Give the extent of all Plasmodium falciparum-infected red blood cells.
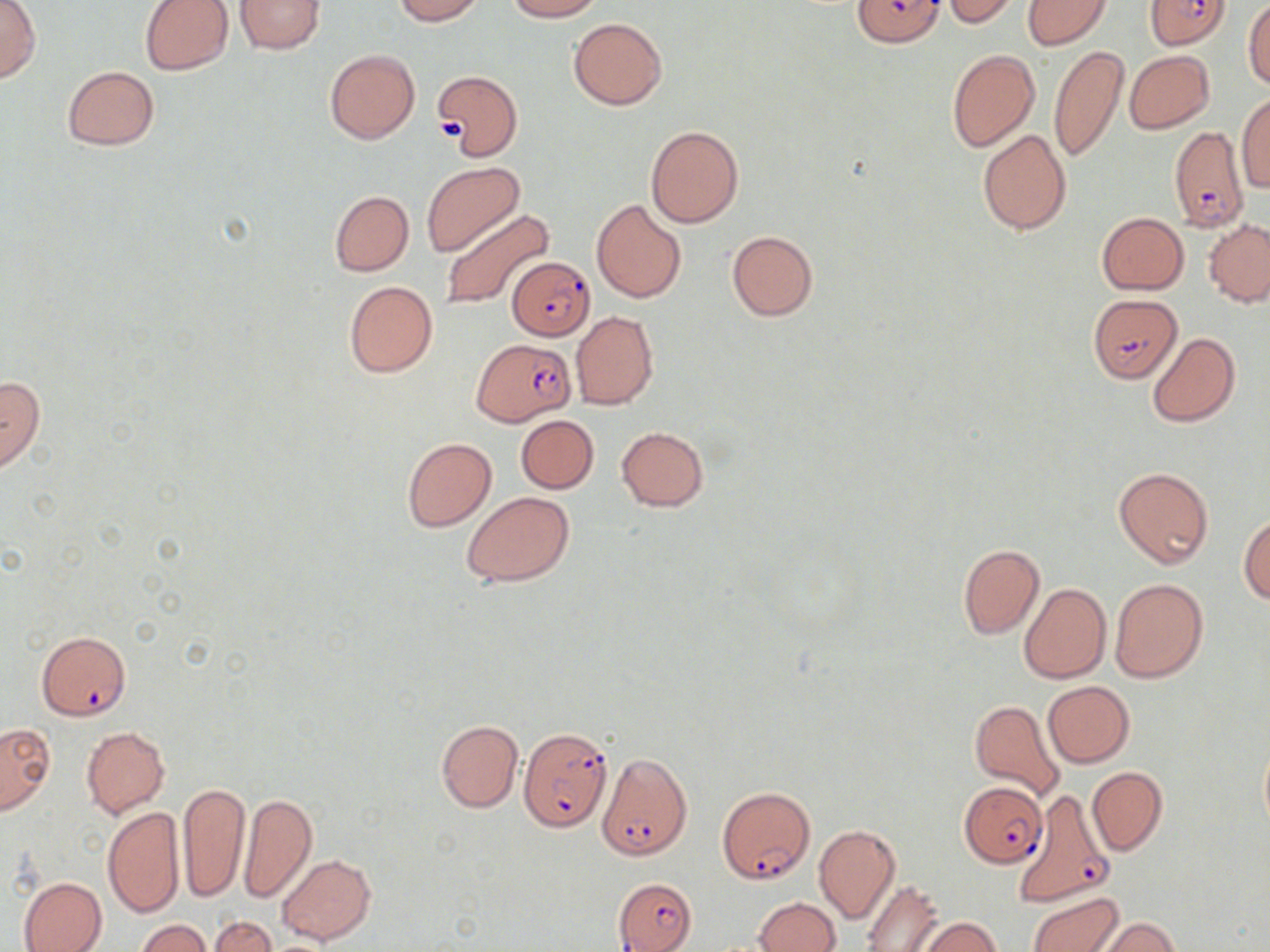
Approximate bounding boxes as (x1,y1)-(x2,y2) corner pairs in pixels.
Plasmodium falciparum-infected red blood cells: (853,0)-(946,47), (1144,0)-(1232,51), (1170,125)-(1248,232), (507,256)-(596,341), (1088,293)-(1185,383), (473,337)-(576,425), (36,630)-(131,721), (519,726)-(612,835), (597,755)-(693,861), (960,782)-(1046,864), (716,784)-(816,885), (1015,788)-(1112,905), (613,877)-(696,952).

slide-level diagnosis = Plasmodium falciparum
field of view = one of a larger specimen
stain = May-Grünwald-Giemsa
uninfected red blood cell locations = approximate bounding boxes as (x1,y1)-(x2,y2) corner pairs in pixels: (234,0)-(326,54), (391,0)-(486,23), (503,0)-(603,22), (1022,0)-(1112,50), (1242,0)-(1270,90), (0,1)-(40,83), (139,1)-(233,74), (941,1)-(1021,26), (568,18)-(667,109), (1048,45)-(1129,164), (325,49)-(420,145), (947,49)-(1039,151), (1124,50)-(1215,134), (62,65)-(160,151), (433,70)-(522,160), (1235,92)-(1270,193), (645,125)-(744,228), (978,129)-(1072,235), (422,162)-(524,256), (328,190)-(414,277), (591,198)-(687,304), (440,209)-(555,311), (1096,211)-(1189,294), (1204,219)-(1270,306), (726,229)-(819,320), (343,281)-(438,378), (571,311)-(658,410), (1148,332)-(1240,428), (0,374)-(45,473), (515,415)-(599,493), (616,427)-(708,512), (402,436)-(496,533), (1114,466)-(1215,570), (461,492)-(575,586), (1239,513)-(1269,604), (957,543)-(1046,640), (1109,578)-(1208,683), (1019,583)-(1111,683), (1042,681)-(1134,767), (969,697)-(1065,804), (436,720)-(523,812), (0,723)-(55,815), (81,726)-(169,818), (1258,740)-(1270,838), (1087,766)-(1167,855), (178,782)-(251,905), (238,792)-(317,903), (102,806)-(185,919), (814,824)-(901,923), (276,853)-(375,946), (18,876)-(107,952), (861,878)-(946,952), (1026,891)-(1122,952), (754,897)-(841,952), (209,916)-(276,952), (909,916)-(1002,952), (1093,916)-(1181,951), (135,919)-(211,952)
preparation = thin blood smear
image size = 1270×952 pixels
magnification = 1000x
platelet locations = approximate bounding boxes as (x1,y1)-(x2,y2) corner pairs in pixels: (436,118)-(462,142)
modality = light microscopy